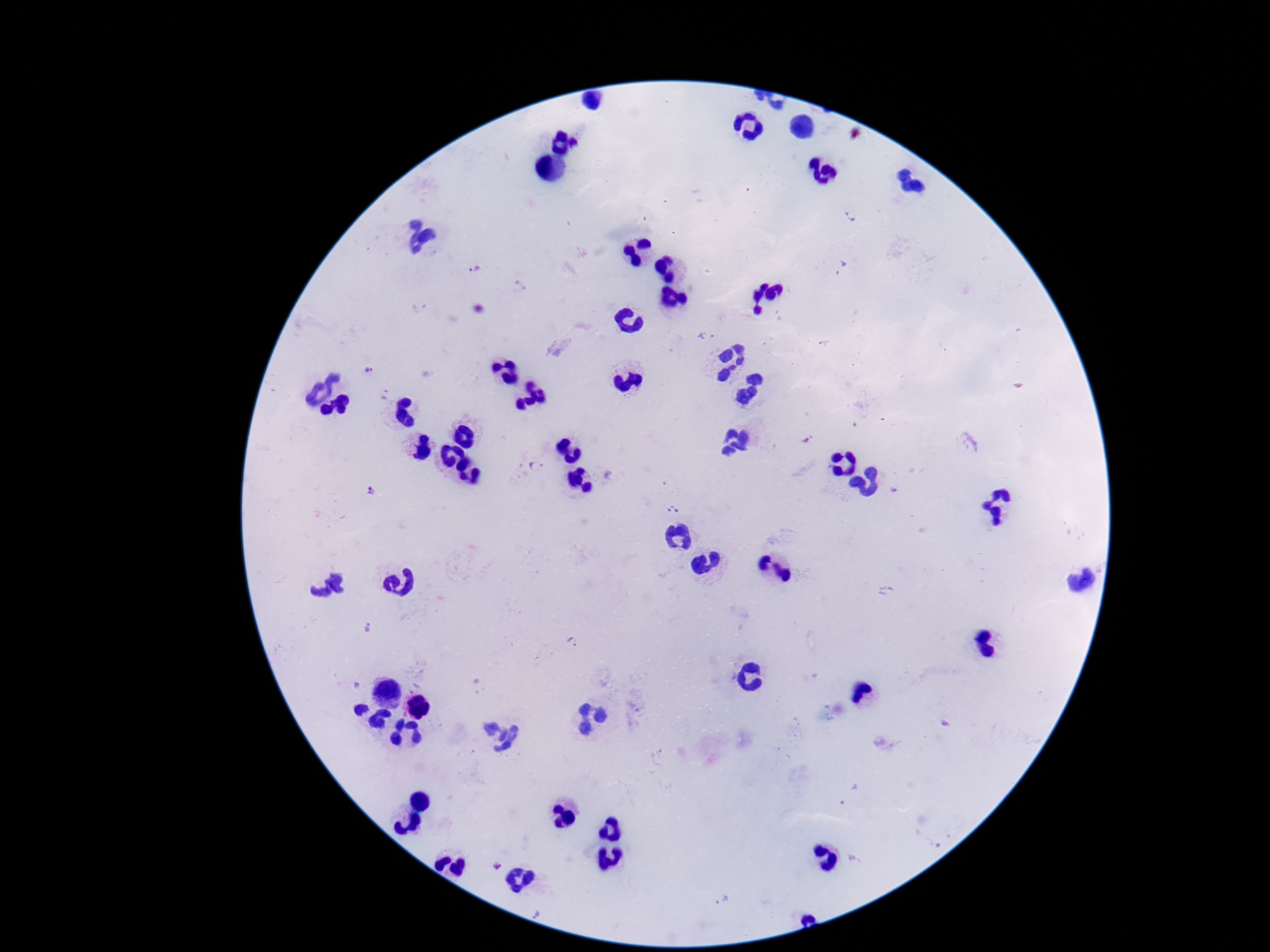

field of view = one from this slide
preparation = thick blood smear
Plasmodium parasite locations = approximate centers as (x, y) in pixels: (852, 216), (842, 268), (474, 269), (705, 337), (369, 369), (384, 394), (807, 440), (537, 466), (374, 490), (675, 510), (886, 591), (367, 628), (575, 641), (658, 758), (495, 863), (724, 898), (540, 913)
image size = 1270×952 pixels
capture = smartphone camera through the microscope eyepiece
stain = Giemsa
magnification = 100x
patient malaria status = positive